State which parasite is depicted.
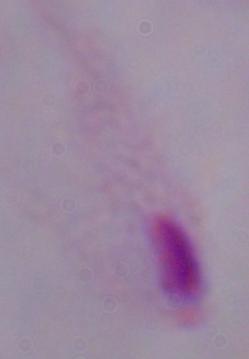

A trichomonad.

1000x magnification. Photomicrograph.